Report the malaria status of this cell.
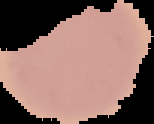
It is uninfected.

image_type: cell region segmented out of the field of view; surrounding area masked to black
image_size: 154×124 pixels
preparation: thin blood film